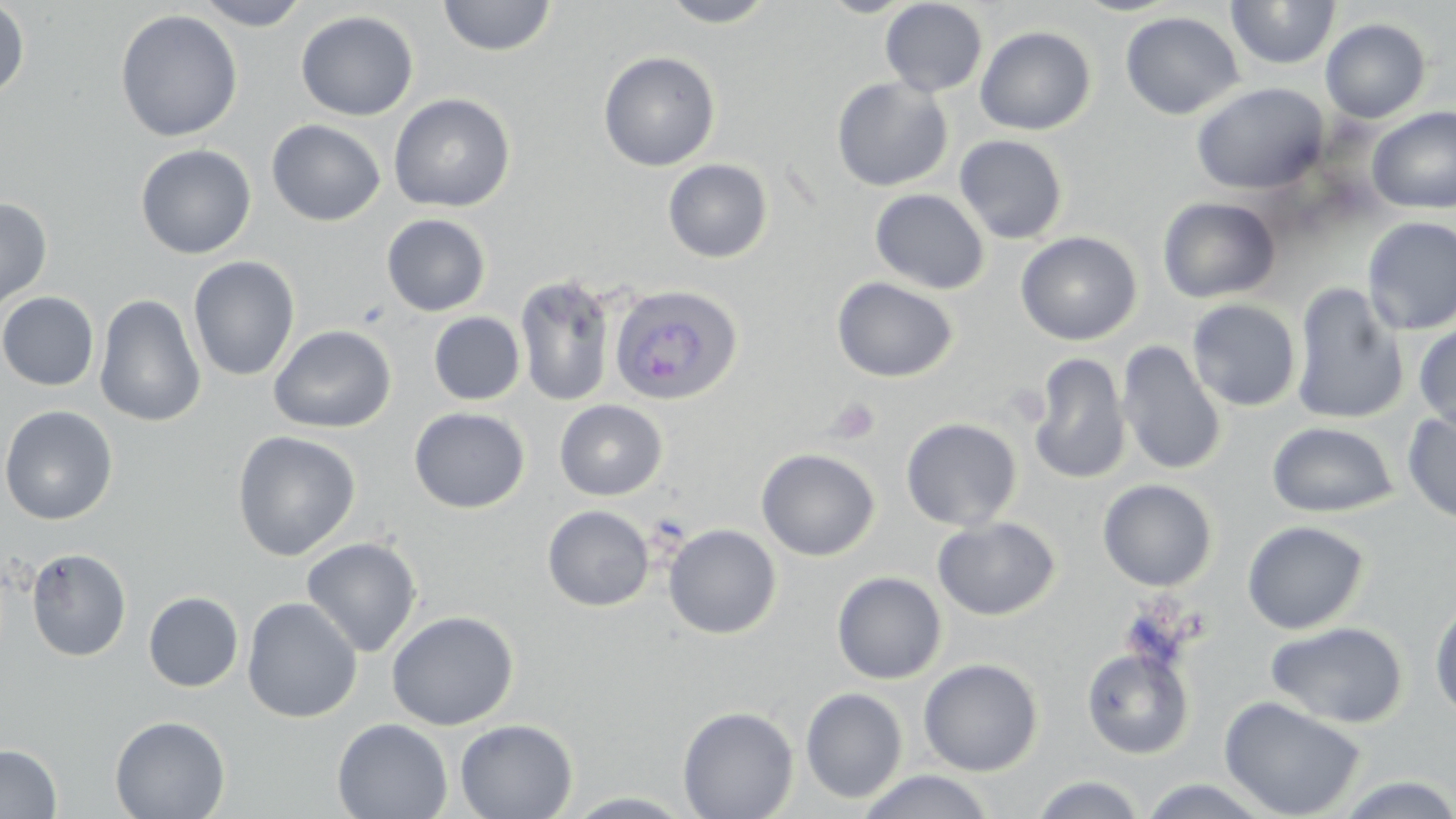
Approximate bounding boxes as [x1, y1, x2, y2] in pixels. Platelet locations: [828, 398, 881, 444]. Uninfected red blood cell locations: [193, 0, 312, 30], [437, 0, 556, 57], [657, 0, 781, 28], [817, 0, 922, 18], [1226, 0, 1341, 70], [880, 1, 988, 98], [0, 2, 30, 101], [114, 9, 243, 143], [296, 10, 419, 121], [1120, 11, 1243, 120], [1320, 18, 1431, 123], [975, 25, 1096, 135], [598, 50, 721, 171], [831, 76, 953, 192], [1191, 82, 1329, 195], [388, 93, 516, 213], [1367, 106, 1456, 214], [266, 119, 386, 226], [954, 134, 1069, 244], [135, 143, 256, 259], [663, 159, 773, 263], [869, 188, 990, 294], [1157, 196, 1281, 303], [0, 197, 53, 312], [381, 213, 491, 316], [1361, 216, 1456, 335], [1015, 231, 1142, 345], [187, 255, 300, 382], [513, 273, 618, 408], [832, 276, 959, 383], [1290, 281, 1409, 426], [0, 291, 99, 391], [94, 293, 207, 427], [1187, 299, 1301, 412], [428, 312, 526, 405], [1413, 322, 1456, 434], [268, 324, 396, 433], [1116, 340, 1226, 476], [1028, 353, 1131, 485], [555, 400, 668, 501], [0, 405, 118, 525], [409, 407, 530, 513], [1402, 408, 1456, 525], [901, 417, 1022, 531], [1267, 421, 1398, 517], [232, 430, 361, 561], [756, 448, 880, 561], [1098, 479, 1217, 591], [543, 505, 654, 612], [932, 516, 1061, 621], [1242, 520, 1370, 634], [663, 523, 782, 639], [301, 536, 422, 657], [26, 547, 132, 662], [832, 571, 947, 684], [143, 591, 244, 692], [1429, 595, 1456, 722], [242, 597, 362, 723], [386, 610, 519, 730], [1266, 621, 1409, 728], [1081, 647, 1194, 759], [919, 658, 1043, 776], [801, 687, 907, 804], [1219, 696, 1367, 819], [677, 706, 799, 819], [110, 715, 230, 819], [332, 717, 453, 818], [455, 718, 578, 818], [0, 743, 62, 819], [857, 770, 996, 819], [1029, 774, 1148, 818], [1329, 774, 1456, 818], [1134, 776, 1279, 818], [562, 791, 699, 817]. Plasmodium ovale-infected red blood cell locations: [608, 284, 743, 406]. Slide-level diagnosis: Plasmodium ovale. Light microscopy. 1000x magnification. Image is 1456×819 pixels. Thin blood smear. May-Grünwald-Giemsa stain. Single field of view.